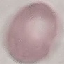
{
  "malaria_status": "uninfected",
  "capture": "smartphone through the microscope eyepiece",
  "stain": "Giemsa",
  "image_type": "cell patch, automatically extracted from a larger field of view and resized to 64 × 64 pixels",
  "preparation": "thin blood smear"
}